Assess this cell for malaria.
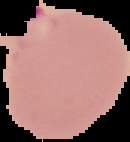

It is parasitized.

preparation = thin blood film
image type = segmented cell region on a black background
image size = 130×142 pixels